State the blood parasite species.
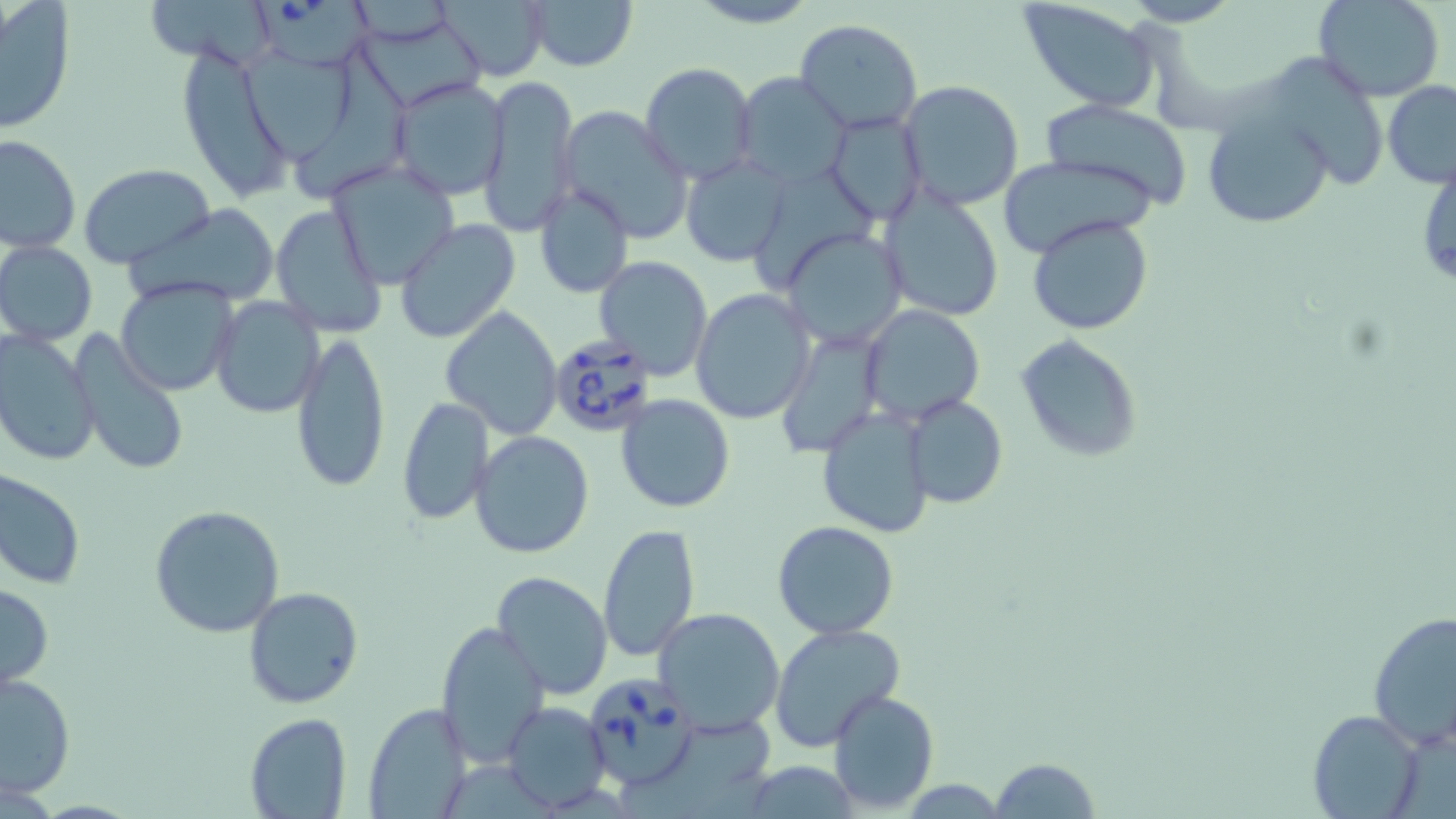
Babesia divergens.

magnification = 1000x
Babesia divergens-infected red blood cell locations = approximate bounding boxes as named x1/y1/x2/y2 corners in pixels: (x1=255, y1=0, x2=377, y2=66), (x1=548, y1=333, x2=660, y2=438), (x1=589, y1=675, x2=699, y2=791)
field of view = one of a larger specimen
stain = May-Grünwald-Giemsa
uninfected red blood cell locations = approximate bounding boxes as named x1/y1/x2/y2 corners in pixels: (x1=149, y1=0, x2=273, y2=69), (x1=434, y1=0, x2=551, y2=82), (x1=526, y1=0, x2=637, y2=71), (x1=688, y1=0, x2=821, y2=29), (x1=1017, y1=0, x2=1162, y2=113), (x1=1121, y1=0, x2=1242, y2=26), (x1=1313, y1=0, x2=1445, y2=101), (x1=1, y1=3, x2=75, y2=133), (x1=794, y1=19, x2=923, y2=134), (x1=359, y1=27, x2=490, y2=110), (x1=305, y1=42, x2=417, y2=195), (x1=246, y1=44, x2=358, y2=165), (x1=175, y1=45, x2=295, y2=204), (x1=1272, y1=54, x2=1388, y2=183), (x1=641, y1=62, x2=757, y2=183), (x1=733, y1=72, x2=848, y2=187), (x1=479, y1=73, x2=578, y2=237), (x1=387, y1=77, x2=511, y2=201), (x1=1382, y1=80, x2=1456, y2=188), (x1=898, y1=81, x2=1025, y2=212), (x1=1039, y1=99, x2=1195, y2=212), (x1=1199, y1=104, x2=1334, y2=231), (x1=556, y1=105, x2=695, y2=243), (x1=826, y1=111, x2=926, y2=226), (x1=0, y1=134, x2=80, y2=254), (x1=680, y1=154, x2=793, y2=265), (x1=995, y1=156, x2=1154, y2=256), (x1=325, y1=158, x2=460, y2=289), (x1=78, y1=164, x2=216, y2=270), (x1=534, y1=182, x2=634, y2=298), (x1=879, y1=189, x2=1005, y2=322), (x1=131, y1=204, x2=280, y2=309), (x1=269, y1=204, x2=387, y2=339), (x1=1027, y1=214, x2=1154, y2=336), (x1=393, y1=219, x2=521, y2=344), (x1=781, y1=226, x2=909, y2=348), (x1=1, y1=242, x2=97, y2=345), (x1=593, y1=256, x2=715, y2=378), (x1=116, y1=279, x2=237, y2=396), (x1=691, y1=290, x2=817, y2=426), (x1=209, y1=296, x2=324, y2=420), (x1=860, y1=304, x2=985, y2=422), (x1=440, y1=306, x2=563, y2=440), (x1=69, y1=329, x2=191, y2=479), (x1=290, y1=329, x2=391, y2=494), (x1=776, y1=329, x2=885, y2=460), (x1=0, y1=330, x2=98, y2=468), (x1=1018, y1=334, x2=1143, y2=464), (x1=615, y1=394, x2=737, y2=512), (x1=902, y1=395, x2=1007, y2=510), (x1=394, y1=396, x2=493, y2=525), (x1=817, y1=405, x2=935, y2=537), (x1=468, y1=430, x2=596, y2=560), (x1=1, y1=468, x2=84, y2=589), (x1=148, y1=504, x2=286, y2=638), (x1=772, y1=521, x2=900, y2=639), (x1=597, y1=523, x2=699, y2=665), (x1=492, y1=570, x2=613, y2=699), (x1=0, y1=581, x2=53, y2=690), (x1=243, y1=586, x2=365, y2=710), (x1=651, y1=606, x2=786, y2=736), (x1=1367, y1=607, x2=1455, y2=754), (x1=436, y1=620, x2=550, y2=766), (x1=768, y1=625, x2=907, y2=755), (x1=0, y1=673, x2=76, y2=797), (x1=827, y1=688, x2=939, y2=812), (x1=501, y1=702, x2=610, y2=811), (x1=363, y1=704, x2=474, y2=816), (x1=1309, y1=708, x2=1425, y2=817), (x1=245, y1=712, x2=351, y2=818), (x1=989, y1=758, x2=1101, y2=817)
modality = light microscopy
image size = 1456×819 pixels
preparation = thin blood film